Identify the parasite.
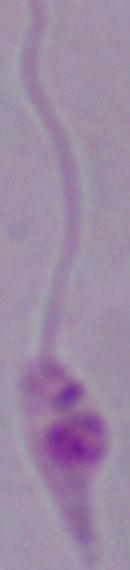

Leishmania.

Micrograph. Captured at 1000x magnification.